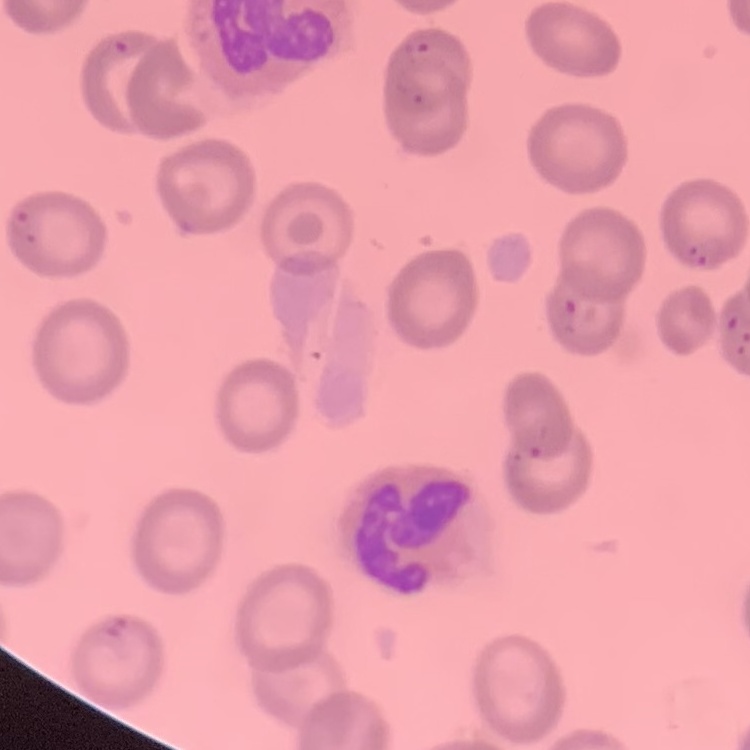
Summary:
  - Red blood cell morphology: no rouleaux formation
  - Image type: square crop of a larger photomicrograph
  - Stain: Field's or Giemsa
  - Preparation: thin peripheral smear